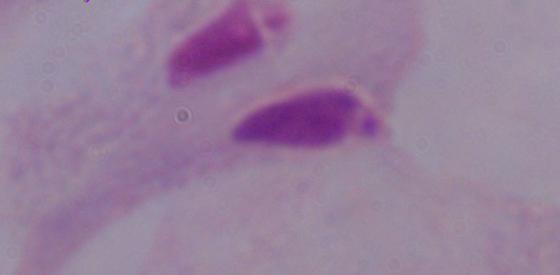
Summary:
  - Identification: trichomonad
  - Magnification: 1000x
  - Modality: micrograph